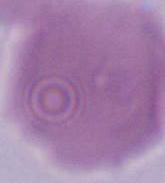

modality: photomicrograph
identification: red blood cell
magnification: 1000x